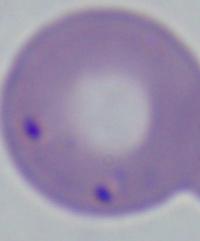

Summary:
  - Modality: photomicrograph
  - Identification: Babesia
  - Magnification: 1000x